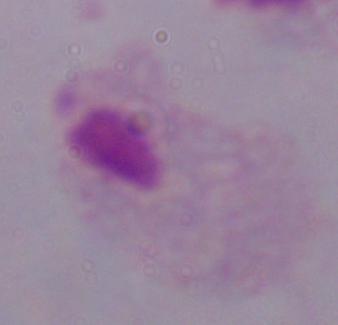

Summary:
  - Magnification: 1000x
  - Identification: trichomonad
  - Modality: photomicrograph